Locate and identify every blood parasite.
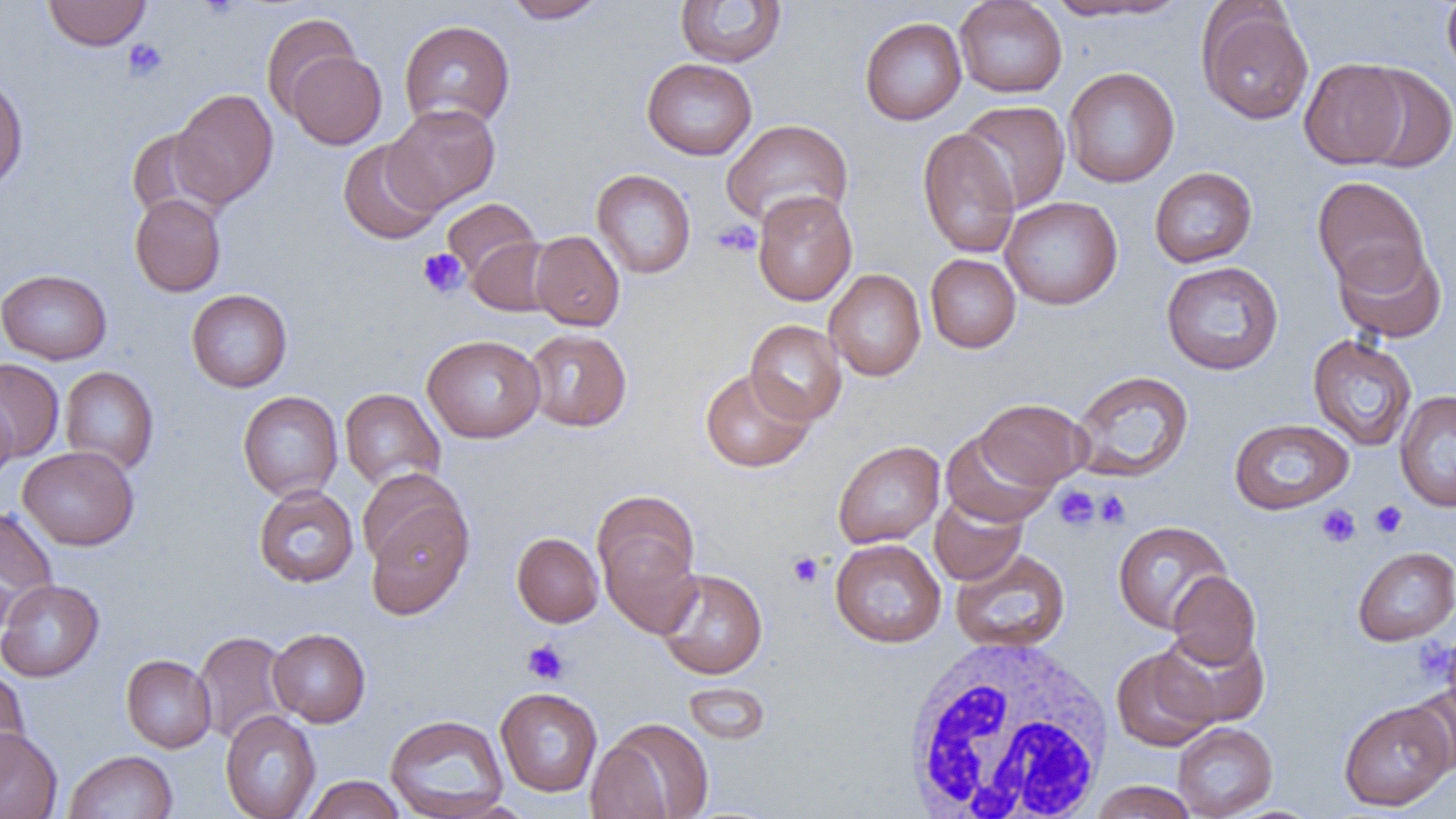

No blood parasites observed.

Approximate bounding boxes as (x1,y1)-(x2,y2) corner pairs in pixels. White blood cell locations: (899,635)-(1118,818). Platelet locations: (122,38)-(168,82), (713,220)-(761,257), (418,248)-(468,298), (1053,485)-(1100,531), (1095,490)-(1131,528), (1370,500)-(1407,538), (1316,504)-(1361,548), (787,552)-(824,588), (1415,638)-(1454,684), (522,639)-(570,684). Uninfected red blood cell locations: (42,0)-(151,51), (502,0)-(608,23), (675,0)-(787,67), (954,0)-(1067,98), (1441,0)-(1456,80), (1043,1)-(1192,22), (1197,3)-(1314,125), (261,13)-(360,117), (859,17)-(967,125), (399,19)-(515,131), (286,50)-(386,150), (642,57)-(757,160), (1299,58)-(1410,168), (1353,63)-(1456,174), (1063,67)-(1179,188), (0,72)-(29,194), (171,88)-(278,209), (957,100)-(1071,213), (384,103)-(500,212), (721,118)-(853,230), (126,128)-(225,222), (917,128)-(1020,258), (338,138)-(443,245), (1149,166)-(1258,267), (591,168)-(696,279), (1312,176)-(1430,292), (752,190)-(857,306), (130,193)-(226,297), (1000,196)-(1123,309), (441,198)-(541,280), (530,230)-(625,331), (466,237)-(558,316), (1332,240)-(1448,344), (925,254)-(1021,353), (1160,261)-(1284,375), (824,268)-(926,381), (0,269)-(112,364), (186,289)-(293,392), (745,319)-(847,426), (522,328)-(632,431), (422,334)-(545,443), (1308,334)-(1417,451), (0,358)-(64,462), (59,366)-(159,474), (700,369)-(816,473), (1070,370)-(1194,483), (340,388)-(446,491), (1395,389)-(1456,512), (238,390)-(343,501), (0,393)-(18,484), (976,398)-(1090,489), (1229,418)-(1353,515), (941,430)-(1055,528), (832,440)-(945,548), (17,446)-(139,550), (358,468)-(467,574), (253,484)-(358,588), (592,489)-(701,597), (929,494)-(1027,585), (365,500)-(473,619), (0,506)-(59,629), (1112,520)-(1233,634), (599,531)-(701,638), (512,532)-(603,627), (830,538)-(946,648), (1353,546)-(1456,645), (950,548)-(1070,653), (656,568)-(768,679), (1166,571)-(1262,670), (0,579)-(104,682), (1152,626)-(1271,729), (268,627)-(371,727), (194,630)-(294,746), (1111,647)-(1219,752), (121,654)-(216,753), (0,666)-(31,783), (683,682)-(771,745), (1405,682)-(1456,776), (495,687)-(603,797), (1338,700)-(1455,811), (220,709)-(321,819), (384,713)-(510,819), (592,717)-(715,819), (1172,723)-(1278,819), (0,728)-(63,819), (63,750)-(178,819), (302,775)-(406,818), (1089,781)-(1198,819). Slide-level diagnosis: no evidence of blood parasites. 1000x magnification. Image is 1456×819 pixels. Thin blood film. Light microscopy. Single field of view.